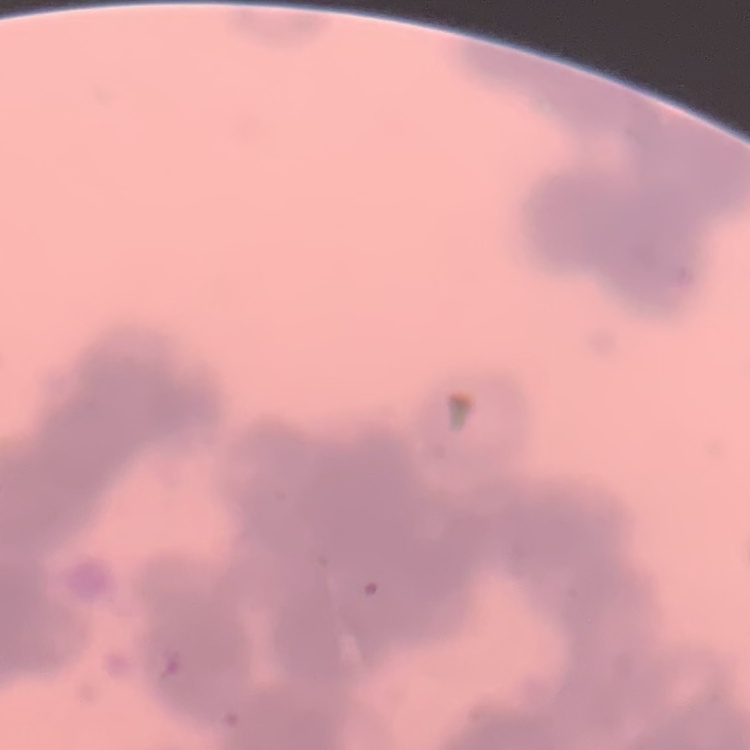

The red blood cells show rouleaux formation. One tile cut from a larger photomicrograph. Thin peripheral smear. Stained with either Field's or Giemsa.